Locate every Plasmodium parasite.
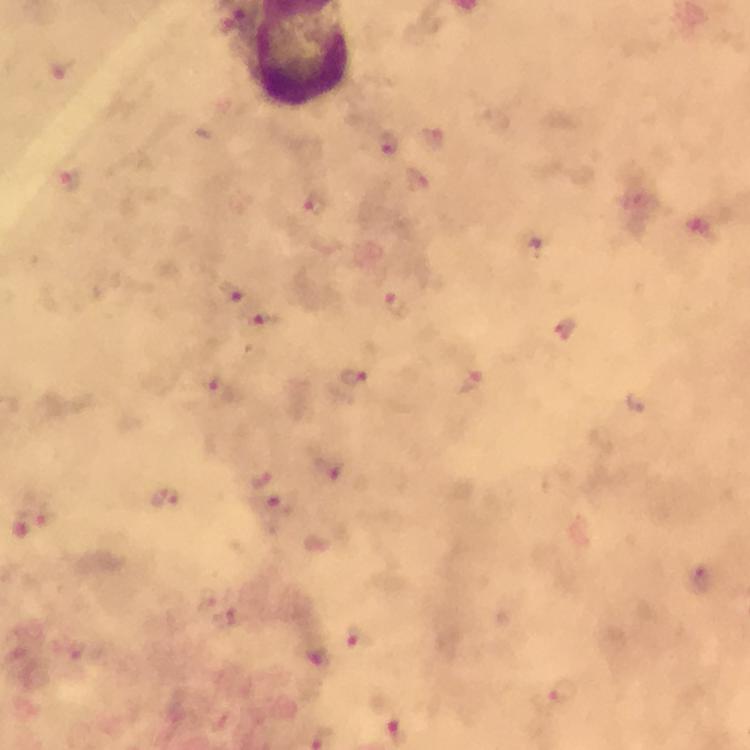
Approximate centers as (x, y) in pixels.
Plasmodium parasites: (58, 68), (565, 691).

Summary:
  - Preparation: thick blood smear
  - Context: from a diagnostic examination for malaria
  - Cropped from: a single field of view
  - Immersion oil: applied
  - Magnification: 100x
  - Stain: Giemsa
  - Image size: 750×750 pixels
  - Capture: smartphone photograph through a microscope